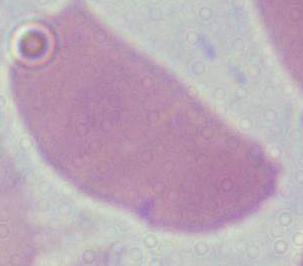

Photomicrograph. Captured at 1000x magnification. A red blood cell is seen.